Point out each Plasmodium parasite.
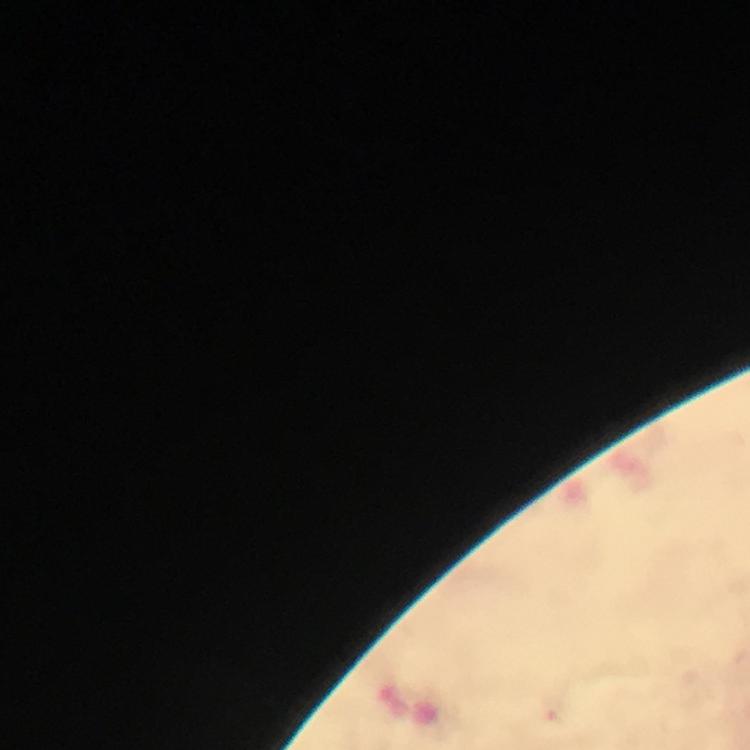
Approximate object centers, in pixels from the top-left corner.
Plasmodium parasites: (x=553, y=710).

magnification = 100x
image size = 750×750 pixels
context = from a malaria diagnostic workup
capture = smartphone camera through the microscope
stain = Giemsa
preparation = thick blood film
cropped from = a single field of view
immersion oil = applied